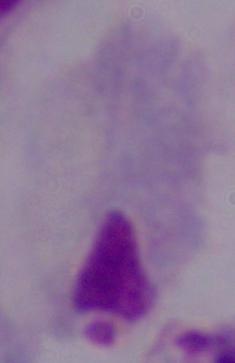
Summary:
  - Identification: trichomonad
  - Modality: micrograph
  - Magnification: 1000x